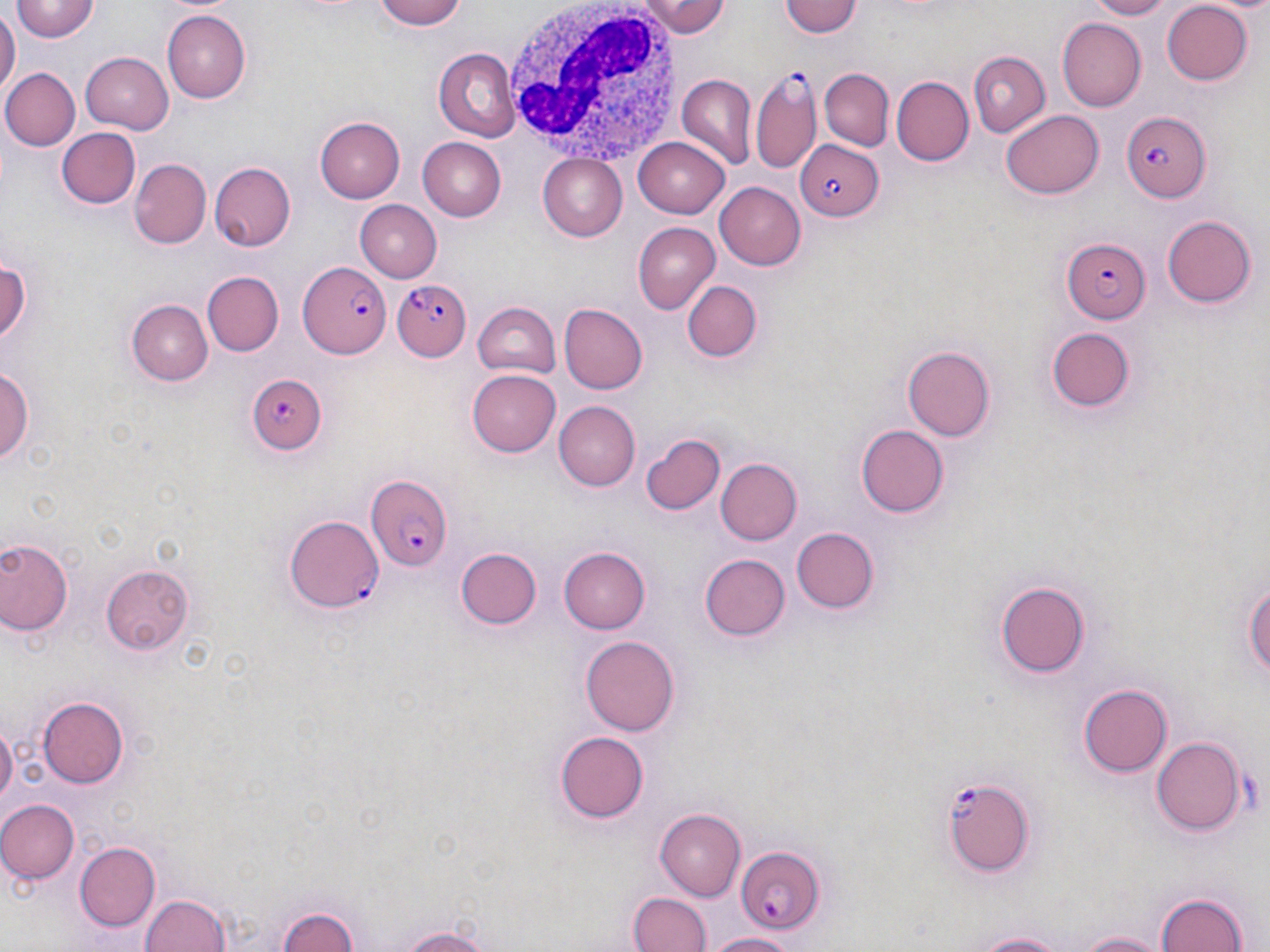
slide_level_diagnosis: Plasmodium falciparum
image_size: 1270×952 pixels
magnification: 1000x
uninfected_red_blood_cell_locations: 'approximate bounding boxes as [x1, y1, x2, y2] in pixels: [377, 0, 469, 29], [647, 0, 731, 38], [778, 0, 863, 39], [1085, 0, 1178, 19], [11, 1, 99, 42], [1161, 1, 1255, 85], [0, 8, 18, 101], [164, 9, 250, 102], [1056, 18, 1146, 111], [431, 46, 520, 143], [965, 49, 1050, 136], [79, 51, 172, 135], [820, 67, 894, 150], [1, 68, 79, 151], [678, 76, 756, 170], [890, 76, 972, 167], [1001, 109, 1103, 199], [314, 116, 402, 203], [57, 127, 141, 208], [634, 136, 732, 218], [419, 138, 505, 221], [536, 153, 627, 241], [130, 159, 209, 248], [209, 160, 298, 251], [714, 182, 807, 270], [355, 201, 443, 282], [1163, 213, 1257, 308], [632, 222, 720, 313], [0, 257, 32, 350], [203, 271, 284, 357], [682, 279, 763, 363], [126, 299, 212, 385], [558, 300, 648, 395], [470, 303, 561, 378], [1047, 327, 1133, 411], [902, 346, 996, 443], [0, 364, 36, 469], [467, 369, 559, 458], [554, 401, 639, 490], [856, 424, 947, 516], [641, 432, 727, 517], [714, 456, 802, 546], [789, 526, 879, 614], [0, 537, 73, 637], [561, 544, 653, 634], [455, 547, 543, 631], [700, 553, 790, 641], [101, 566, 195, 652], [1244, 572, 1270, 691], [995, 580, 1090, 679], [579, 636, 681, 737], [1078, 683, 1175, 778], [38, 696, 131, 788], [0, 718, 17, 809], [552, 729, 649, 822], [1152, 738, 1244, 836], [0, 799, 78, 883], [656, 808, 746, 900], [74, 841, 160, 930], [1152, 888, 1253, 952], [137, 890, 233, 952], [629, 891, 710, 952], [274, 903, 363, 951], [384, 920, 506, 952], [957, 927, 1084, 951], [1070, 928, 1173, 951], [703, 931, 803, 951]'
white_blood_cell_locations: 'approximate bounding boxes as [x1, y1, x2, y2] in pixels: [503, 0, 684, 165]'
field_of_view: single
stain: May-Grünwald-Giemsa
plasmodium_falciparum_infected_red_blood_cell_locations: 'approximate bounding boxes as [x1, y1, x2, y2] in pixels: [750, 69, 823, 177], [1121, 111, 1210, 203], [794, 139, 884, 219], [1061, 240, 1151, 322], [295, 258, 390, 363], [395, 280, 475, 359], [247, 373, 329, 455], [368, 477, 454, 572], [286, 513, 386, 614], [940, 776, 1038, 877], [733, 845, 826, 932]'
modality: optical microscopy
preparation: thin blood smear